Give the position of every Plasmodium parasite visible.
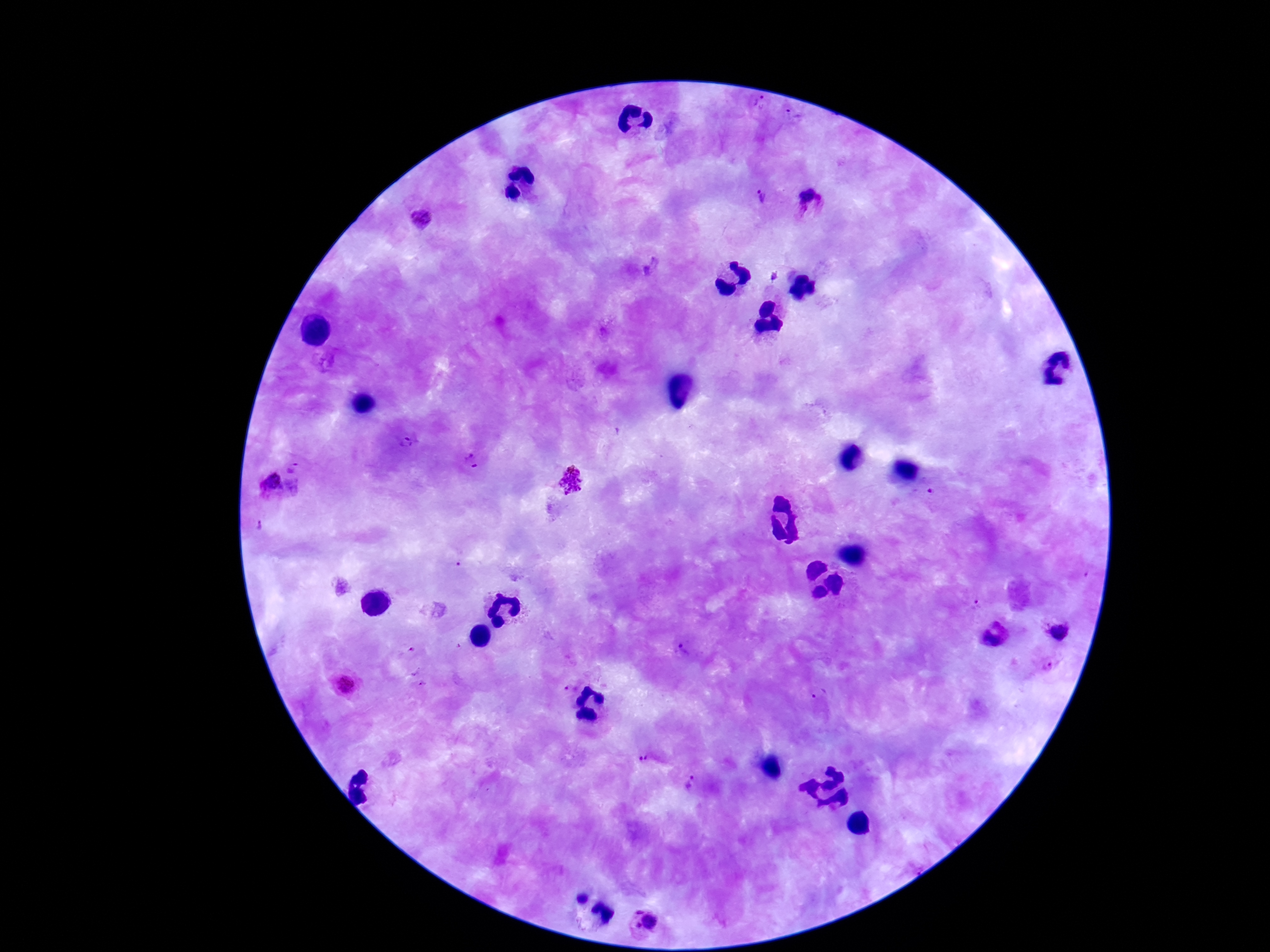
Approximate centers as [x, y] in pixels.
Plasmodium parasites: [756, 108], [796, 121], [756, 200], [807, 207], [422, 219], [774, 274], [406, 445], [472, 463], [294, 465], [573, 481], [268, 492], [1058, 631], [410, 653], [349, 685], [423, 685], [569, 689], [817, 694], [644, 760], [695, 784], [644, 923].

Giemsa stain. Image is 1270×952 pixels. Single field of view. Smartphone photograph taken through the microscope eyepiece. 100x magnification. Thick blood smear. Patient malaria status: positive.